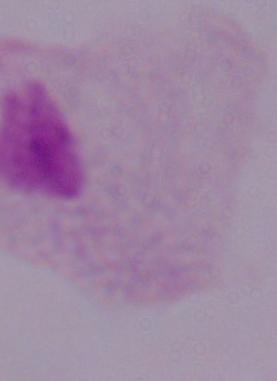 1000x magnification. Photomicrograph. A trichomonad is shown.